State which parasite is depicted.
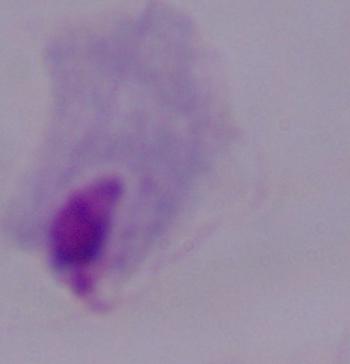
This is a trichomonad.

magnification = 1000x
modality = micrograph